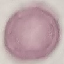

Summary:
  - Malaria status: uninfected
  - Capture: smartphone camera at the microscope eyepiece
  - Preparation: thin smear
  - Image type: automatically extracted cell patch, resized to 64 × 64 pixels
  - Stain: Giemsa